Assess this cell for malaria.
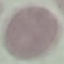
It is uninfected.

stain = Giemsa
preparation = thin smear
image type = automatically extracted cell patch, resized to 64 × 64 pixels
capture = smartphone camera at the microscope eyepiece